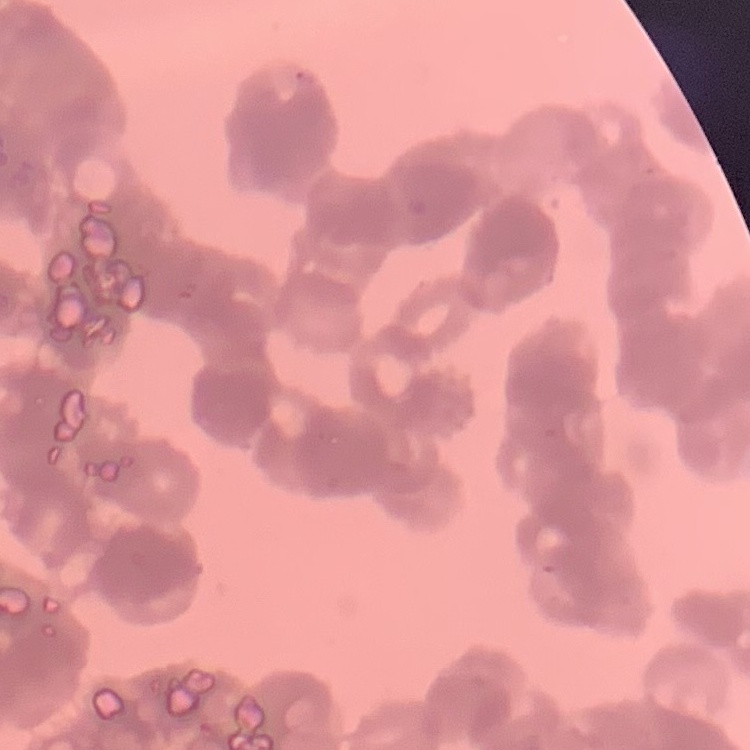
The erythrocytes show rouleaux formation. One tile cut from a larger photomicrograph. Thin blood smear. Field's or Giemsa stain.